Identify the parasite.
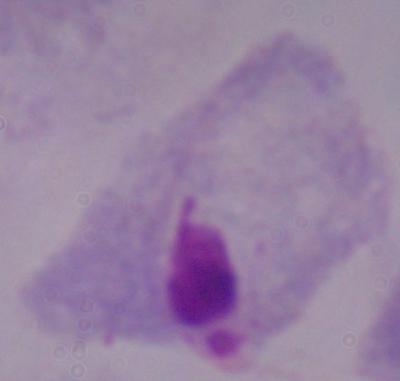
This is a trichomonad.

modality = micrograph
magnification = 1000x